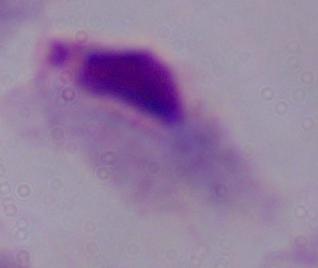
magnification: 1000x
modality: photomicrograph
identification: trichomonad